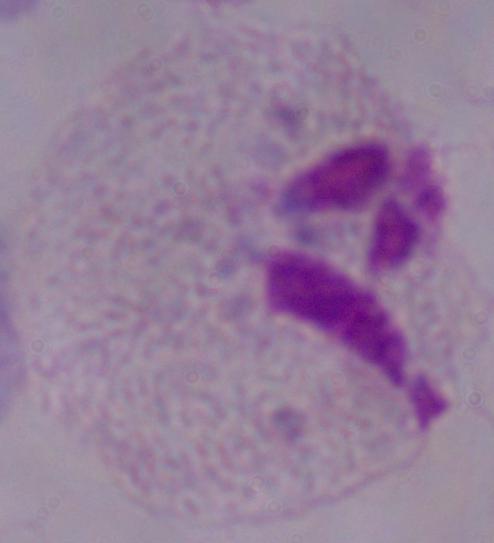

Summary:
  - Modality: micrograph
  - Identification: trichomonad
  - Magnification: 1000x